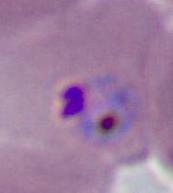
Photomicrograph. 400x or 1000x magnification. A Plasmodium parasite is shown.